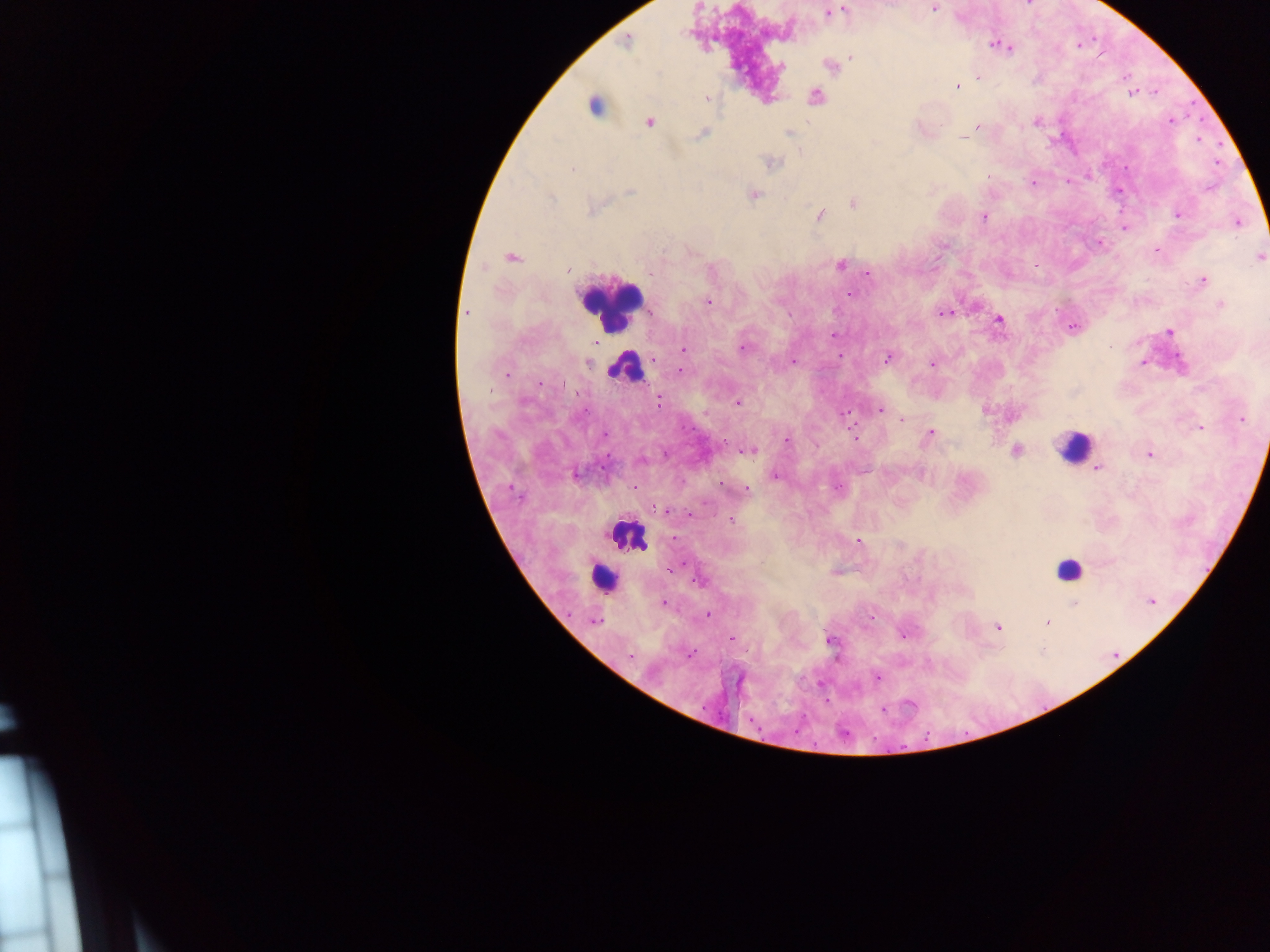

Approximate centers as x y in pixels. Leukocyte locations: 610 306; 626 368; 1073 446; 625 536; 1068 568; 603 579. Plasmodium parasite locations: 933 9; 844 10; 829 13; 627 41; 996 46; 1009 48; 851 57; 781 67; 978 77; 957 86; 1131 94; 816 97; 707 98; 593 107; 1170 120; 649 122; 1035 122; 978 127; 789 133; 701 134; 963 138; 772 163; 572 168; 988 175; 1032 183; 630 191; 753 194; 552 198; 853 203; 592 209; 821 215; 1178 215; 984 216; 1238 223; 1125 227; 1156 250; 512 257; 1259 258; 841 264; 567 269; 649 274; 868 274; 1203 280; 850 294; 707 302; 1221 304; 466 312; 944 313; 999 319; 1073 328; 1169 332; 832 335; 742 348; 683 350; 840 355; 888 358; 793 362; 1142 363; 588 364; 931 364; 681 372; 508 373; 562 384; 659 402; 737 403; 879 410; 845 412; 1241 419; 902 420; 1199 428; 931 433; 604 435; 854 437; 786 441; 751 451; 1016 451; 1150 454; 1097 468; 576 475; 776 475; 745 490; 659 508; 665 510; 732 520; 858 541; 674 569; 701 581; 663 602; 1151 602; 1074 603; 708 615; 595 621; 1048 622; 998 628; 903 635; 732 639; 830 640; 689 654; 630 656; 877 678. One field of view. Collected in Ghana. Image is 1270×952 pixels. Mobile-phone photograph taken through the microscope. Thick blood smear.